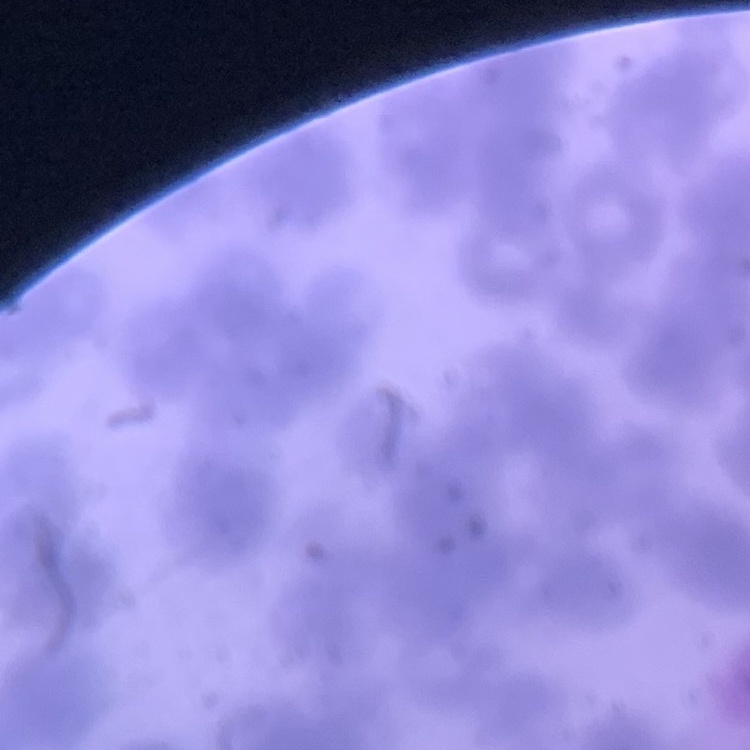

The red blood cells exhibit rouleaux formation. Stained with either Field's or Giemsa. Thin blood smear. One tile cut from a larger photomicrograph.